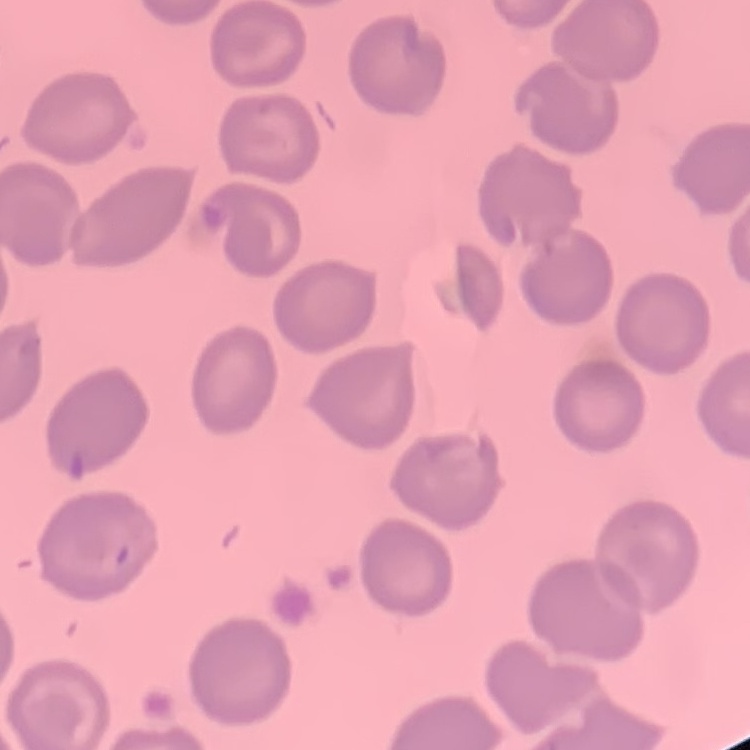 The erythrocytes show no rouleaux formation. One tile cut from a larger photomicrograph. Thin peripheral smear. Stained with either Field's or Giemsa.